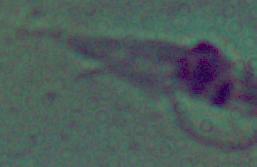

{
  "modality": "micrograph",
  "identification": "Leishmania",
  "magnification": "1000x"
}